Name the blood parasite species.
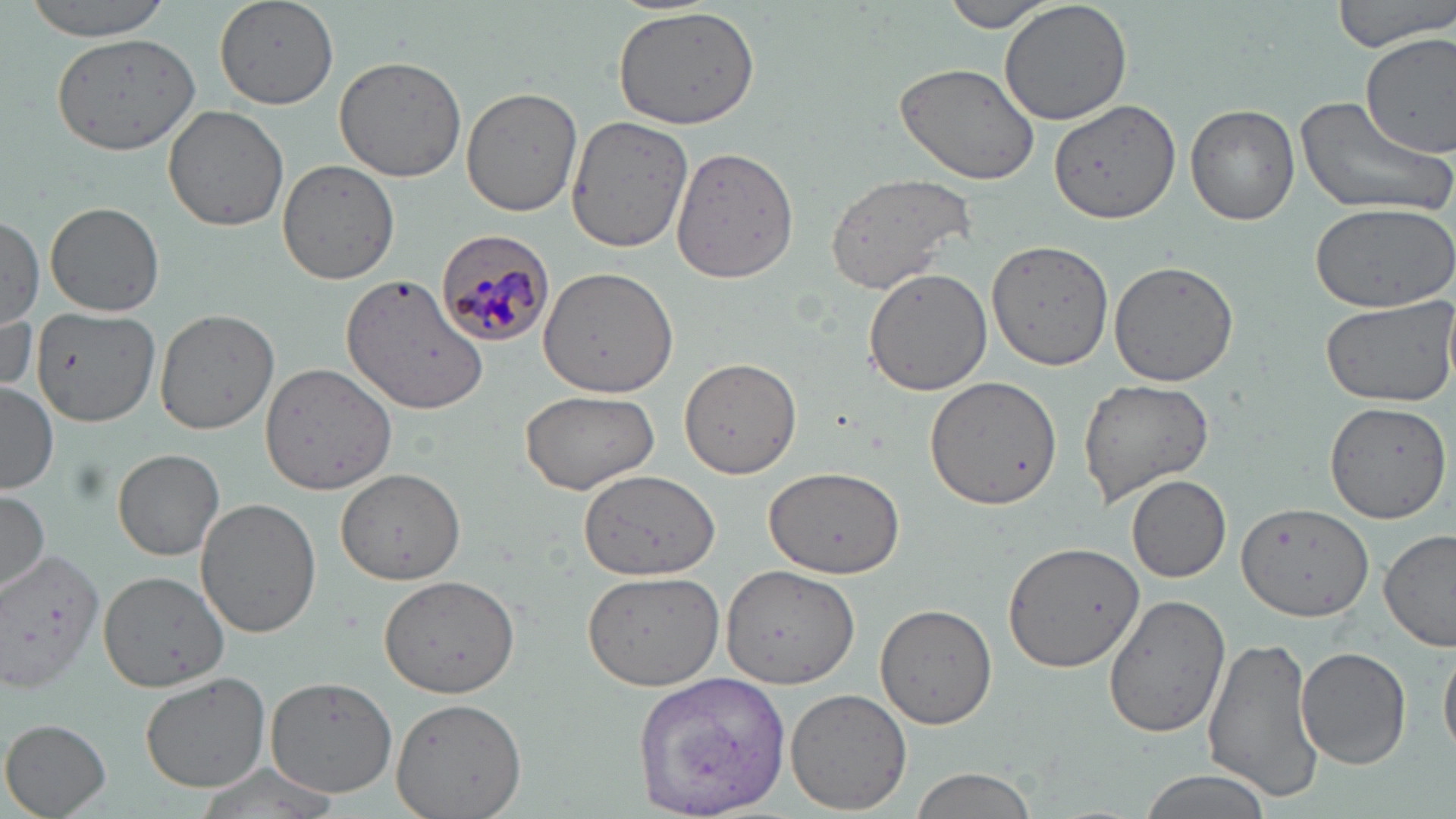
Plasmodium malariae.

{
  "stain": "May-Grünwald-Giemsa",
  "preparation": "thin blood film",
  "magnification": "1000x",
  "plasmodium_malariae_infected_red_blood_cell_locations": "approximate bounding boxes as (x1, y1, x2, y2) in pixels: (434, 226, 556, 349)",
  "uninfected_red_blood_cell_locations": "approximate bounding boxes as (x1, y1, x2, y2) in pixels: (23, 0, 173, 39), (216, 0, 339, 109), (942, 0, 1062, 32), (998, 0, 1135, 131), (1333, 0, 1454, 54), (612, 5, 762, 130), (1357, 31, 1454, 156), (49, 32, 200, 155), (335, 55, 466, 181), (895, 61, 1043, 186), (460, 87, 583, 216), (1295, 94, 1454, 219), (1049, 101, 1180, 224), (164, 103, 291, 231), (1186, 104, 1299, 226), (565, 116, 695, 253), (670, 146, 800, 286), (276, 159, 400, 283), (824, 171, 979, 295), (1309, 200, 1455, 313), (45, 201, 165, 318), (0, 216, 45, 327), (984, 238, 1113, 371), (1108, 260, 1242, 388), (539, 266, 676, 397), (863, 268, 992, 396), (343, 274, 488, 413), (1320, 294, 1456, 408), (31, 306, 162, 424), (153, 309, 280, 436), (679, 359, 801, 477), (260, 361, 399, 496), (925, 376, 1061, 509), (1077, 378, 1215, 506), (1, 381, 60, 492), (519, 388, 661, 493), (1324, 402, 1452, 523), (113, 448, 225, 561), (763, 464, 906, 579), (334, 468, 468, 586), (578, 470, 721, 582), (1126, 474, 1233, 583), (0, 490, 50, 593), (196, 497, 322, 638), (1236, 500, 1373, 622), (1380, 529, 1456, 653), (1004, 542, 1145, 670), (0, 548, 104, 695), (721, 567, 858, 689), (97, 569, 230, 691), (579, 569, 727, 692), (377, 575, 521, 696), (1100, 595, 1229, 739), (875, 604, 998, 729), (1205, 636, 1324, 802), (1440, 639, 1456, 766), (1295, 646, 1412, 769), (141, 673, 272, 792), (634, 673, 790, 816), (265, 677, 399, 797), (785, 686, 913, 813), (390, 695, 527, 818), (2, 718, 112, 817), (190, 760, 344, 819), (907, 767, 1038, 819), (1134, 770, 1277, 819)",
  "field_of_view": "one of a larger specimen",
  "image_size": "1456×819 pixels",
  "modality": "light microscopy"
}